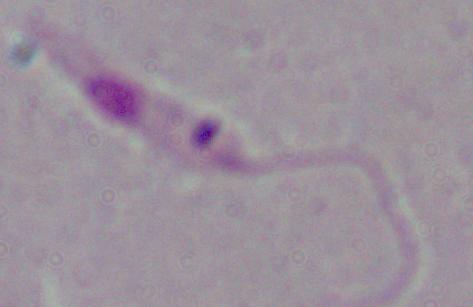
Summary:
  - Identification: Leishmania
  - Modality: photomicrograph
  - Magnification: 1000x